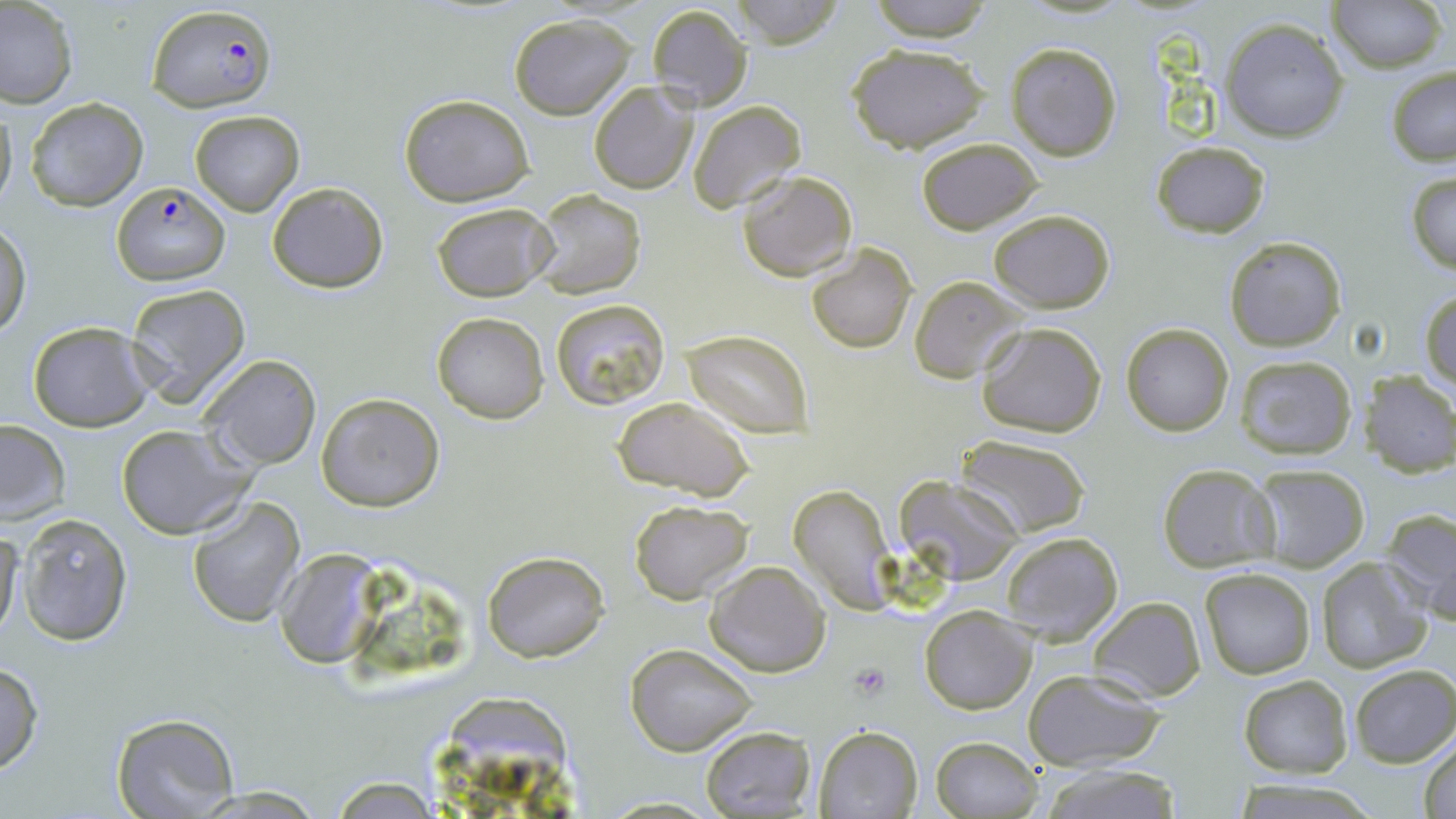

slide_level_diagnosis: Plasmodium falciparum
image_size: 1456×819 pixels
modality: light microscopy
plasmodium_falciparum_infected_red_blood_cell_locations: 'approximate bounding boxes as (x1, y1, x2, y2) in pixels: (147, 4, 277, 112), (112, 183, 230, 284)'
uninfected_red_blood_cell_locations: 'approximate bounding boxes as (x1, y1, x2, y2) in pixels: (730, 0, 847, 48), (861, 0, 998, 42), (1329, 0, 1445, 73), (0, 2, 78, 108), (646, 4, 752, 113), (508, 14, 636, 119), (1220, 18, 1351, 142), (1005, 42, 1122, 163), (845, 43, 991, 151), (1386, 66, 1456, 166), (588, 83, 700, 195), (398, 94, 534, 206), (25, 97, 148, 210), (688, 100, 807, 212), (0, 101, 17, 214), (189, 109, 304, 215), (914, 137, 1044, 236), (1152, 141, 1270, 237), (1405, 169, 1456, 275), (736, 170, 857, 282), (266, 182, 389, 293), (530, 188, 646, 299), (433, 202, 553, 301), (987, 209, 1115, 312), (1, 221, 30, 337), (1224, 236, 1347, 352), (806, 243, 917, 352), (909, 276, 1025, 383), (124, 283, 251, 408), (1421, 291, 1456, 392), (551, 298, 671, 412), (432, 312, 550, 423), (28, 320, 152, 431), (976, 322, 1107, 439), (1120, 322, 1234, 436), (684, 329, 813, 437), (198, 353, 322, 471), (1233, 354, 1358, 460), (1364, 371, 1455, 477), (316, 392, 444, 512), (610, 396, 755, 500), (0, 420, 69, 523), (114, 424, 253, 539), (956, 434, 1091, 535), (1157, 464, 1280, 570), (1253, 464, 1370, 569), (897, 474, 1025, 586), (789, 484, 898, 613), (186, 495, 306, 627), (628, 501, 754, 604), (1380, 506, 1456, 622), (18, 512, 134, 646), (0, 528, 24, 642), (1000, 531, 1123, 645), (274, 550, 385, 666), (481, 550, 611, 662), (1318, 558, 1435, 673), (705, 561, 830, 678), (1199, 568, 1318, 679), (1089, 596, 1206, 703), (919, 606, 1036, 713), (625, 643, 757, 756), (0, 661, 44, 776), (1350, 664, 1456, 767), (1022, 669, 1166, 771), (1239, 675, 1352, 777), (445, 695, 572, 798), (110, 712, 239, 818), (813, 724, 923, 818), (699, 726, 815, 817), (1417, 733, 1456, 819), (930, 735, 1044, 819), (1038, 763, 1186, 819), (327, 777, 447, 816), (596, 796, 727, 817)'
magnification: 1000x
stain: May-Grünwald-Giemsa
preparation: thin blood smear
platelet_locations: 'approximate bounding boxes as (x1, y1, x2, y2) in pixels: (846, 662, 892, 701)'
field_of_view: one of a larger specimen